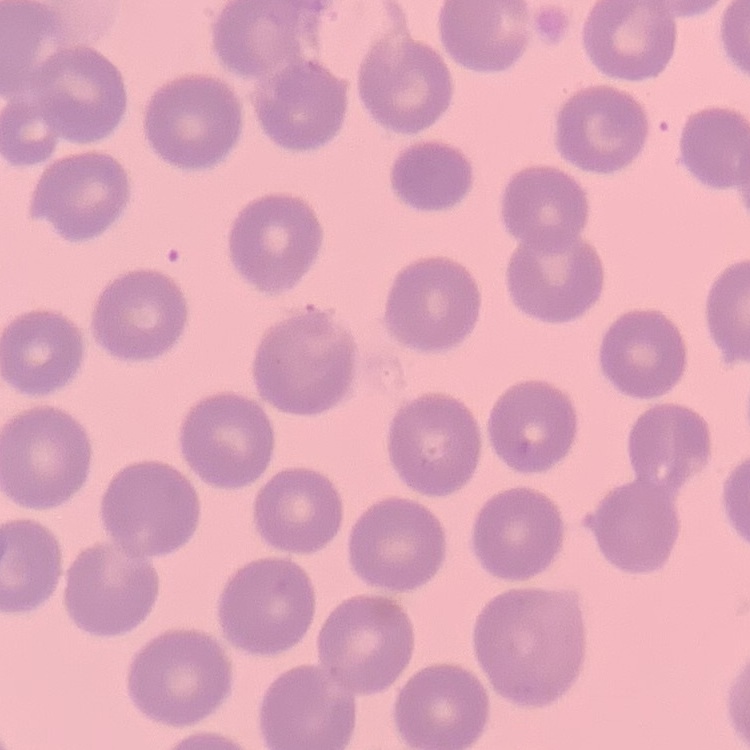

The erythrocytes show no rouleaux formation. Field's or Giemsa stain. Thin blood smear. One tile cut from a larger photomicrograph.